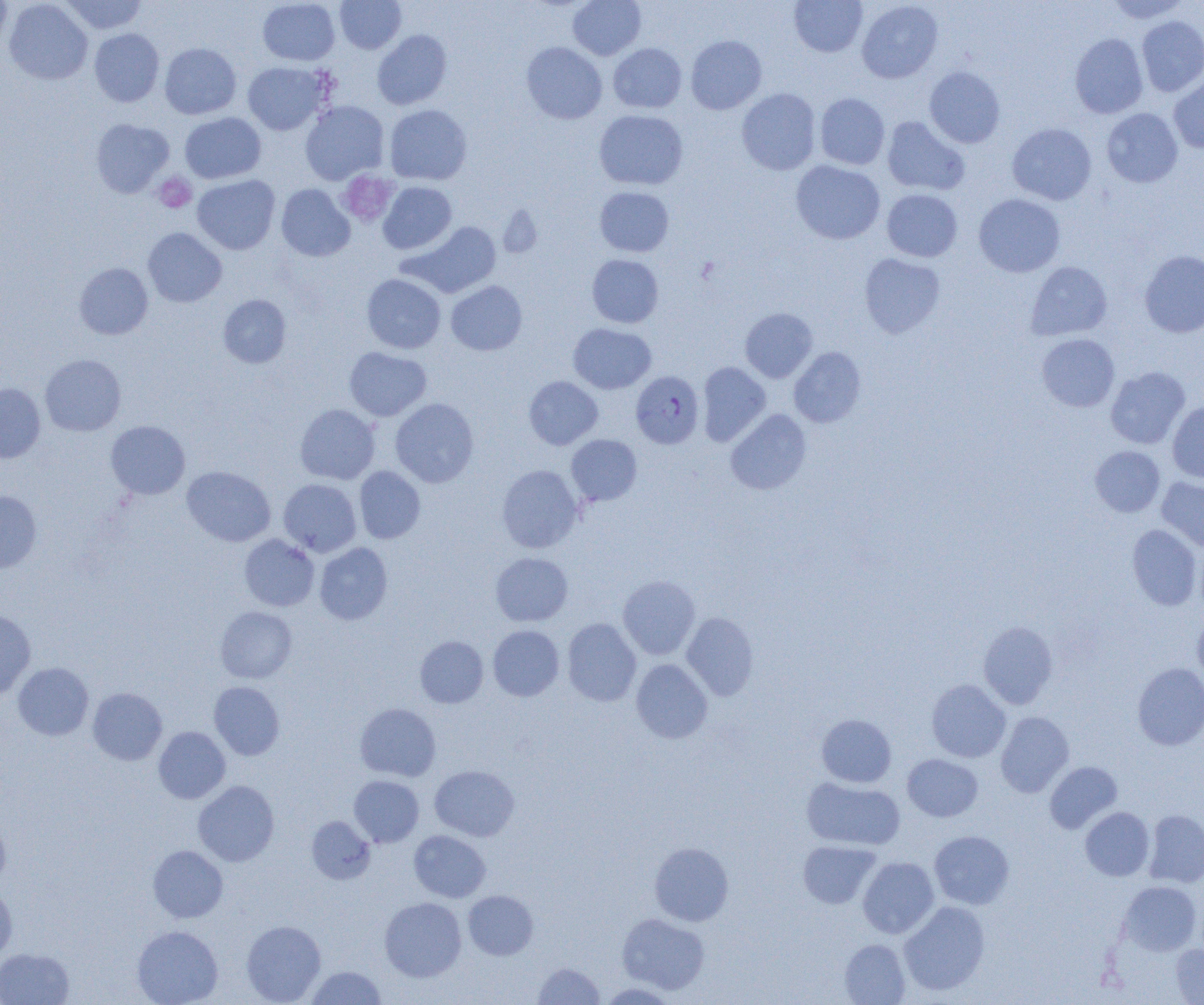
slide-level diagnosis = Plasmodium falciparum
modality = optical microscopy
image size = 1204×1005 pixels
uninfected red blood cell locations = approximate bounding boxes as (x1, y1, x2, y2) in pixels: (0, 0, 12, 56), (4, 0, 93, 85), (60, 0, 147, 34), (258, 0, 340, 66), (335, 0, 406, 53), (568, 0, 646, 60), (789, 0, 868, 57), (1104, 0, 1190, 23), (857, 1, 943, 83), (1136, 15, 1204, 96), (89, 29, 164, 107), (372, 30, 452, 110), (1070, 33, 1148, 118), (686, 35, 766, 114), (521, 42, 607, 124), (160, 43, 241, 119), (608, 43, 687, 113), (243, 62, 331, 135), (924, 66, 1005, 148), (1169, 74, 1204, 153), (737, 88, 821, 175), (815, 93, 890, 170), (300, 101, 389, 184), (384, 104, 472, 185), (1102, 108, 1183, 188), (594, 110, 688, 190), (180, 112, 266, 184), (882, 116, 970, 196), (91, 119, 174, 198), (1007, 123, 1096, 205), (791, 160, 885, 244), (192, 175, 280, 254), (378, 182, 457, 254), (276, 184, 355, 262), (595, 186, 674, 257), (882, 189, 963, 262), (973, 194, 1065, 277), (406, 221, 501, 297), (143, 228, 227, 307), (1139, 250, 1204, 337), (859, 253, 945, 338), (587, 254, 664, 328), (1026, 261, 1112, 340), (74, 262, 153, 340), (362, 274, 446, 354), (446, 281, 527, 355), (218, 294, 291, 368), (740, 307, 818, 383), (568, 323, 656, 394), (1037, 333, 1119, 412), (344, 347, 431, 421), (788, 347, 866, 428), (40, 354, 126, 436), (697, 362, 771, 446), (1105, 366, 1190, 449), (524, 376, 603, 449), (0, 383, 45, 462), (390, 398, 478, 487), (1167, 401, 1204, 483), (295, 404, 380, 484), (726, 409, 811, 494), (106, 421, 190, 499), (566, 435, 642, 505), (1090, 445, 1165, 517), (497, 465, 582, 553), (182, 466, 275, 546), (354, 466, 425, 543), (1157, 477, 1204, 553), (279, 479, 361, 556), (0, 491, 42, 573), (1127, 524, 1201, 610), (239, 534, 319, 611), (315, 543, 392, 625), (490, 552, 573, 626), (618, 575, 700, 659), (215, 606, 297, 683), (0, 609, 35, 700), (1193, 610, 1204, 687), (681, 612, 759, 700), (562, 618, 641, 706), (978, 621, 1058, 709), (488, 625, 564, 701), (415, 635, 488, 708), (631, 658, 713, 744), (13, 663, 93, 740), (1132, 663, 1204, 750), (927, 679, 1010, 762), (209, 681, 285, 760), (88, 688, 167, 765), (355, 703, 440, 781), (996, 711, 1074, 797), (816, 714, 897, 787), (153, 726, 230, 804), (902, 754, 984, 822), (1044, 761, 1122, 833), (430, 765, 519, 841), (349, 775, 423, 847), (802, 777, 905, 851), (193, 780, 279, 866), (1080, 807, 1154, 881), (1143, 810, 1204, 887), (307, 816, 375, 884), (0, 817, 10, 891), (409, 830, 490, 902), (929, 830, 1014, 909), (798, 840, 880, 909), (649, 842, 733, 926), (148, 845, 228, 923), (858, 857, 939, 938), (1119, 881, 1201, 955), (0, 887, 17, 961), (463, 890, 538, 960), (379, 897, 466, 981), (898, 901, 990, 995), (617, 913, 710, 995), (241, 920, 326, 1005), (132, 925, 223, 1005), (839, 938, 910, 1005), (1170, 944, 1204, 1004), (0, 948, 74, 1005), (533, 961, 605, 1004), (305, 966, 386, 1005), (599, 982, 677, 1004)
magnification = 1000x
preparation = thin blood smear
Plasmodium falciparum-infected red blood cell locations = approximate bounding boxes as (x1, y1, x2, y2) in pixels: (631, 371, 704, 449)
field of view = one of a larger specimen
platelet locations = approximate bounding boxes as (x1, y1, x2, y2) in pixels: (338, 171, 398, 226), (153, 173, 196, 213)